Assess this cell for malaria.
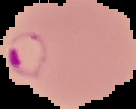

It is parasitized.

Summary:
  - Image type: segmented cell region on a black background
  - Preparation: thin blood film
  - Image size: 136×109 pixels